Name the blood parasite species.
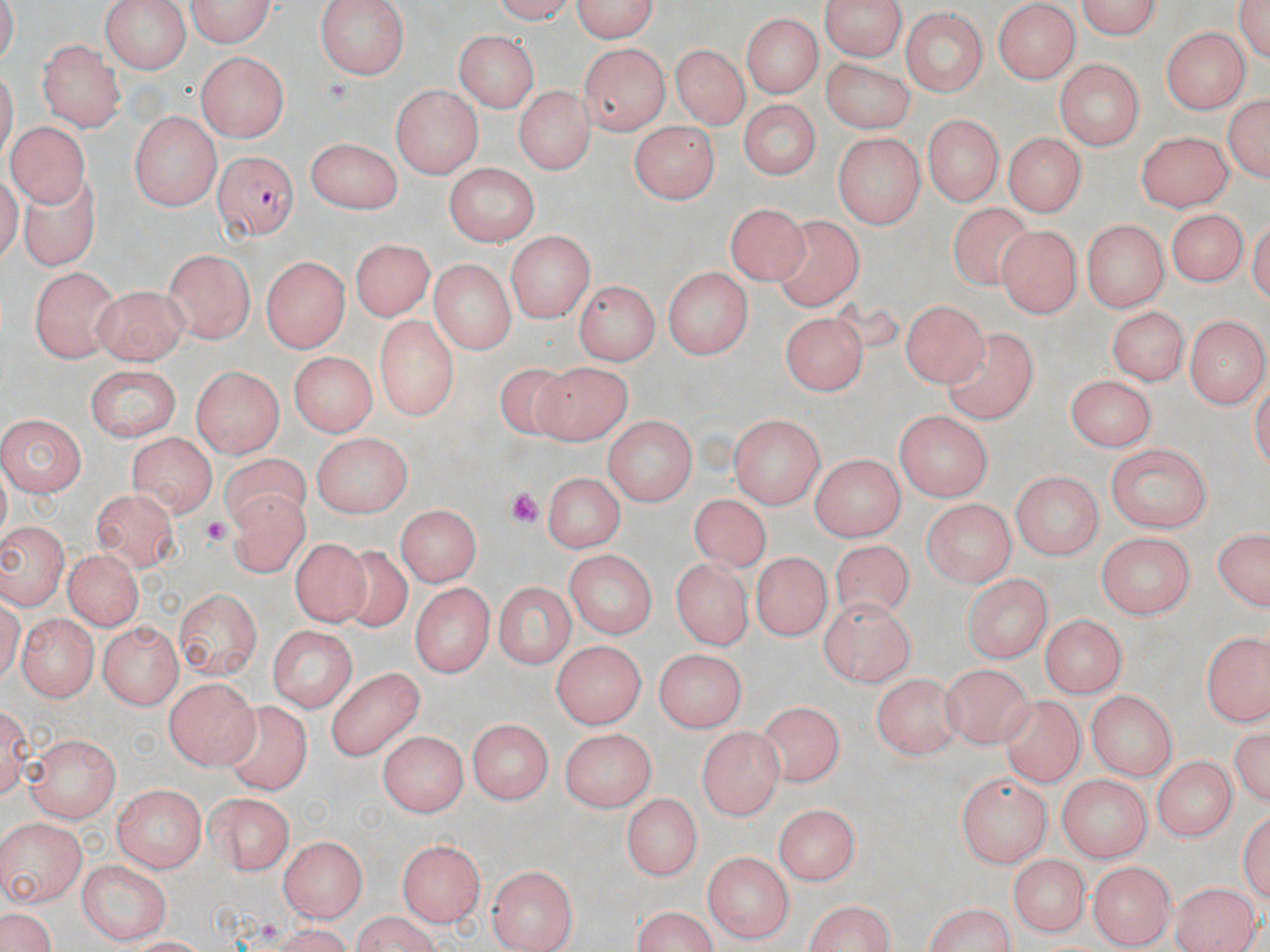

Plasmodium falciparum.

Approximate bounding boxes as (x1, y1, x2, y2) in pixels. Plasmodium falciparum-infected red blood cell locations: (213, 149, 296, 240). Platelet locations: (506, 487, 544, 533), (202, 515, 237, 548). Uninfected red blood cell locations: (99, 0, 190, 75), (179, 0, 279, 48), (316, 0, 408, 77), (563, 0, 661, 41), (824, 0, 904, 62), (1068, 0, 1167, 38), (1230, 0, 1270, 65), (994, 4, 1080, 82), (899, 9, 988, 96), (743, 10, 823, 97), (1162, 29, 1247, 112), (451, 31, 538, 112), (40, 38, 127, 132), (578, 41, 669, 135), (670, 43, 750, 130), (194, 54, 289, 140), (824, 55, 914, 134), (1057, 59, 1143, 152), (514, 82, 593, 172), (389, 85, 479, 177), (1222, 89, 1269, 186), (742, 100, 815, 180), (131, 112, 222, 207), (924, 113, 1004, 205), (6, 121, 98, 214), (633, 122, 718, 204), (1138, 129, 1231, 210), (833, 131, 923, 226), (1002, 134, 1083, 217), (305, 137, 402, 216), (445, 162, 540, 247), (19, 166, 102, 273), (724, 196, 810, 281), (948, 198, 1032, 291), (1167, 206, 1250, 287), (777, 216, 868, 313), (1084, 220, 1165, 312), (995, 225, 1078, 317), (504, 231, 591, 324), (350, 240, 432, 324), (161, 249, 256, 341), (262, 255, 351, 353), (429, 259, 515, 353), (663, 265, 751, 361), (28, 267, 116, 365), (576, 279, 657, 367), (92, 286, 185, 369), (902, 297, 989, 386), (1106, 304, 1187, 385), (781, 312, 867, 394), (1185, 312, 1266, 404), (374, 314, 458, 422), (943, 326, 1037, 423), (290, 353, 374, 440), (534, 362, 630, 442), (495, 363, 581, 447), (82, 364, 182, 439), (192, 365, 285, 457), (1066, 377, 1155, 449), (895, 408, 991, 500), (0, 413, 85, 497), (732, 414, 825, 509), (605, 417, 696, 508), (311, 432, 413, 518), (130, 433, 215, 518), (1105, 443, 1213, 532), (219, 454, 317, 529), (810, 454, 905, 541), (1011, 470, 1100, 558), (545, 471, 621, 554), (231, 484, 307, 580), (92, 488, 178, 570), (689, 494, 772, 579), (924, 498, 1016, 586), (393, 506, 479, 587), (0, 520, 67, 612), (1210, 525, 1268, 615), (1094, 532, 1197, 617), (294, 537, 367, 627), (832, 540, 917, 628), (336, 544, 416, 633), (563, 547, 655, 638), (752, 547, 834, 639), (61, 549, 142, 632), (673, 558, 751, 648), (963, 573, 1056, 660), (493, 579, 574, 669), (409, 582, 495, 680), (173, 584, 261, 681), (820, 597, 916, 685), (14, 611, 95, 702), (1038, 613, 1128, 697), (100, 618, 184, 706), (265, 623, 361, 710), (1201, 629, 1270, 728), (549, 638, 644, 730), (656, 647, 750, 728), (939, 665, 1040, 749), (324, 667, 430, 755), (870, 673, 955, 759), (164, 675, 259, 767), (1086, 692, 1177, 778), (1000, 697, 1088, 793), (758, 699, 844, 790), (223, 700, 311, 791), (468, 717, 553, 805), (1232, 725, 1270, 809), (699, 726, 783, 818), (560, 730, 654, 808), (381, 731, 466, 818), (25, 734, 117, 822), (1150, 756, 1237, 842), (953, 767, 1051, 866), (1057, 773, 1152, 863), (111, 786, 207, 870), (205, 792, 293, 874), (623, 793, 699, 883), (770, 802, 863, 885), (2, 819, 85, 909), (278, 835, 365, 920), (397, 837, 487, 925), (703, 850, 791, 942), (1006, 854, 1091, 937), (78, 859, 171, 945), (487, 862, 577, 950), (1087, 862, 1177, 944), (1172, 878, 1260, 952), (801, 897, 898, 952), (920, 902, 1018, 952), (629, 907, 722, 952), (1, 909, 57, 952), (347, 914, 443, 950), (263, 925, 359, 952). Thin blood film. May-Grünwald-Giemsa stain. Image is 1270×952 pixels. Single field of view. Captured at 1000x magnification. Optical microscopy.